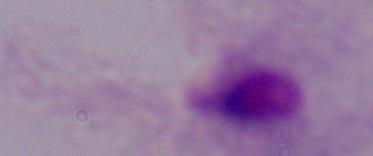 Photomicrograph. A trichomonad is seen. 1000x magnification.